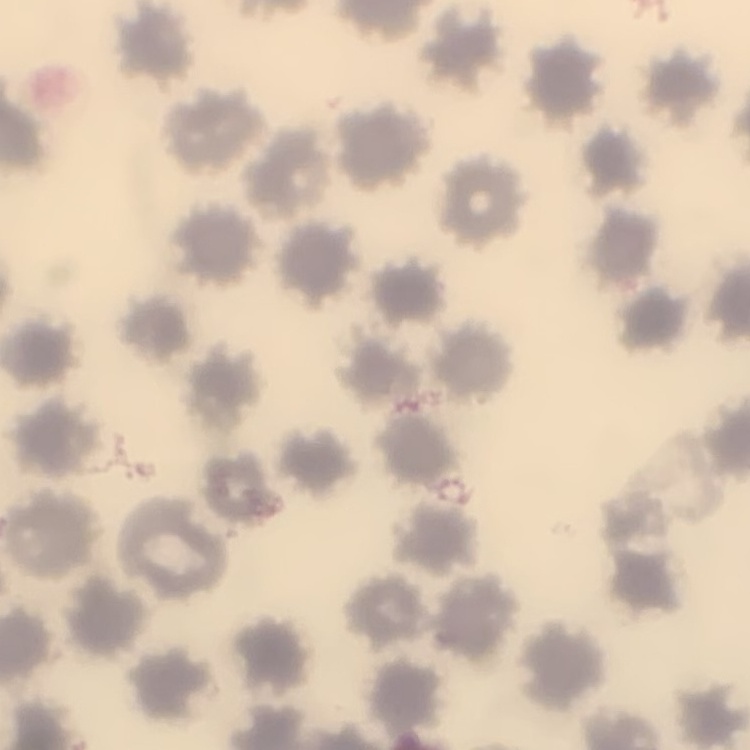

The erythrocytes show no rouleaux formation. Field's or Giemsa stain. One tile cut from a larger photomicrograph. Thin blood film.